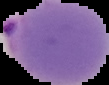

Image is 109×85 pixels. The area outside the segmented cell region is set to black. From a thin blood film. Malaria status: parasitized.